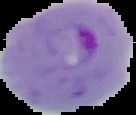
result: malaria parasites detected
image_size: 136×115 pixels
preparation: thin blood smear
image_type: segmented cell region on a black background